Name the parasite shown.
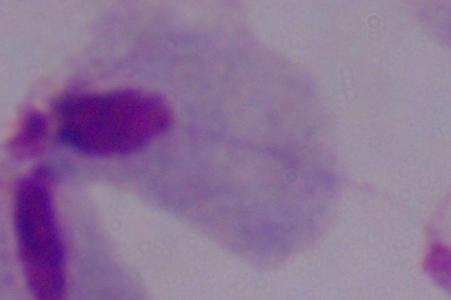
This is a trichomonad.

Summary:
  - Modality: photomicrograph
  - Magnification: 1000x